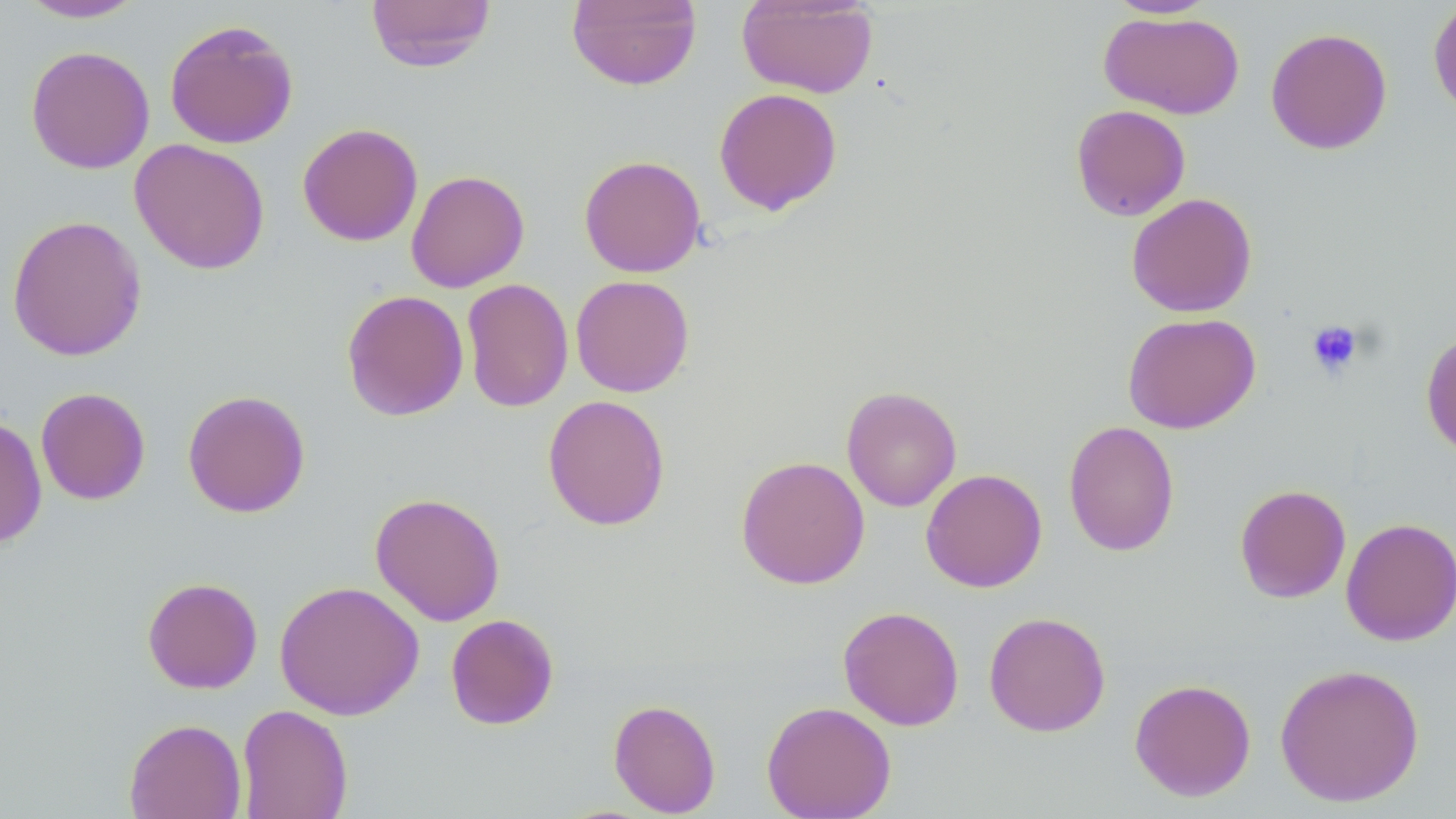
slide_level_diagnosis: no evidence of blood parasites
preparation: thin blood smear
stain: May-Grünwald-Giemsa
uninfected_red_blood_cell_locations: 'approximate bounding boxes as named x1/y1/x2/y2 corners in pixels: (x1=366, y1=0, x2=496, y2=72), (x1=566, y1=0, x2=702, y2=90), (x1=737, y1=0, x2=878, y2=98), (x1=1104, y1=0, x2=1219, y2=19), (x1=1428, y1=0, x2=1456, y2=121), (x1=15, y1=1, x2=148, y2=23), (x1=1099, y1=11, x2=1245, y2=120), (x1=164, y1=19, x2=299, y2=149), (x1=1265, y1=27, x2=1393, y2=154), (x1=25, y1=45, x2=155, y2=174), (x1=714, y1=87, x2=842, y2=215), (x1=1071, y1=104, x2=1191, y2=221), (x1=297, y1=122, x2=423, y2=246), (x1=130, y1=138, x2=270, y2=275), (x1=579, y1=154, x2=706, y2=277), (x1=406, y1=170, x2=529, y2=293), (x1=1126, y1=193, x2=1257, y2=317), (x1=6, y1=214, x2=147, y2=361), (x1=570, y1=274, x2=695, y2=397), (x1=461, y1=278, x2=574, y2=413), (x1=341, y1=289, x2=469, y2=421), (x1=1122, y1=312, x2=1261, y2=434), (x1=1421, y1=330, x2=1456, y2=459), (x1=35, y1=386, x2=151, y2=505), (x1=841, y1=386, x2=962, y2=511), (x1=182, y1=389, x2=311, y2=518), (x1=542, y1=394, x2=671, y2=531), (x1=0, y1=416, x2=47, y2=550), (x1=1063, y1=420, x2=1180, y2=557), (x1=736, y1=455, x2=870, y2=589), (x1=920, y1=468, x2=1047, y2=593), (x1=1234, y1=483, x2=1351, y2=603), (x1=370, y1=492, x2=505, y2=626), (x1=1340, y1=517, x2=1456, y2=647), (x1=142, y1=576, x2=263, y2=694), (x1=274, y1=580, x2=424, y2=720), (x1=838, y1=605, x2=964, y2=730), (x1=983, y1=611, x2=1111, y2=737), (x1=445, y1=613, x2=559, y2=730), (x1=1274, y1=662, x2=1425, y2=807), (x1=1129, y1=678, x2=1256, y2=801), (x1=608, y1=698, x2=721, y2=816), (x1=761, y1=700, x2=896, y2=819), (x1=236, y1=703, x2=353, y2=819), (x1=124, y1=718, x2=247, y2=819)'
modality: light microscopy
image_size: 1456×819 pixels
platelet_locations: 'approximate bounding boxes as named x1/y1/x2/y2 corners in pixels: (x1=1306, y1=320, x2=1364, y2=379)'
field_of_view: single
magnification: 1000x